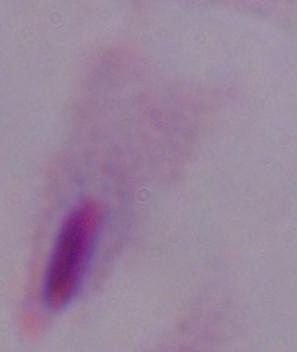

Summary:
  - Modality: photomicrograph
  - Identification: trichomonad
  - Magnification: 1000x